Assess the morphology of the erythrocytes.
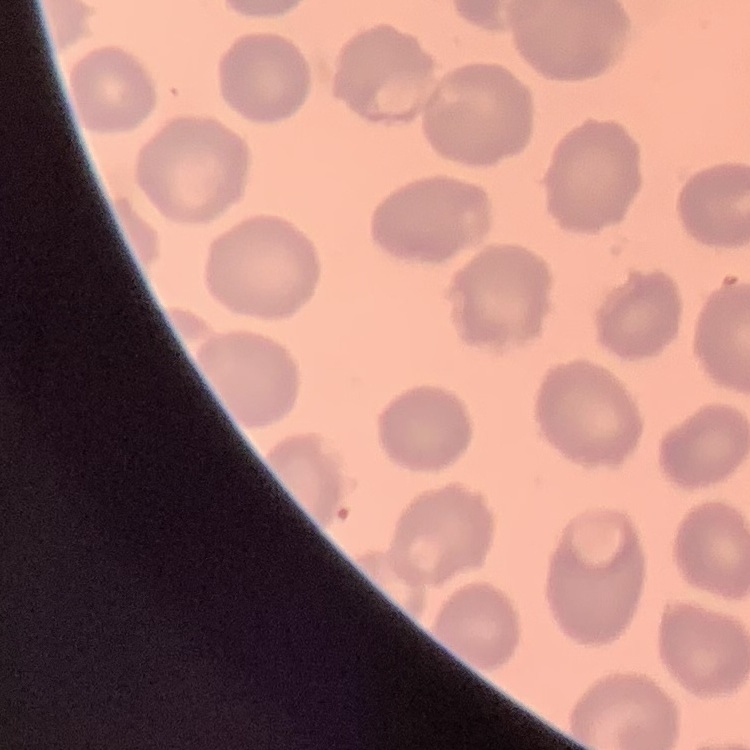
They show no rouleaux formation.

Square crop of a larger photomicrograph. Stained with either Field's or Giemsa. Thin blood smear.